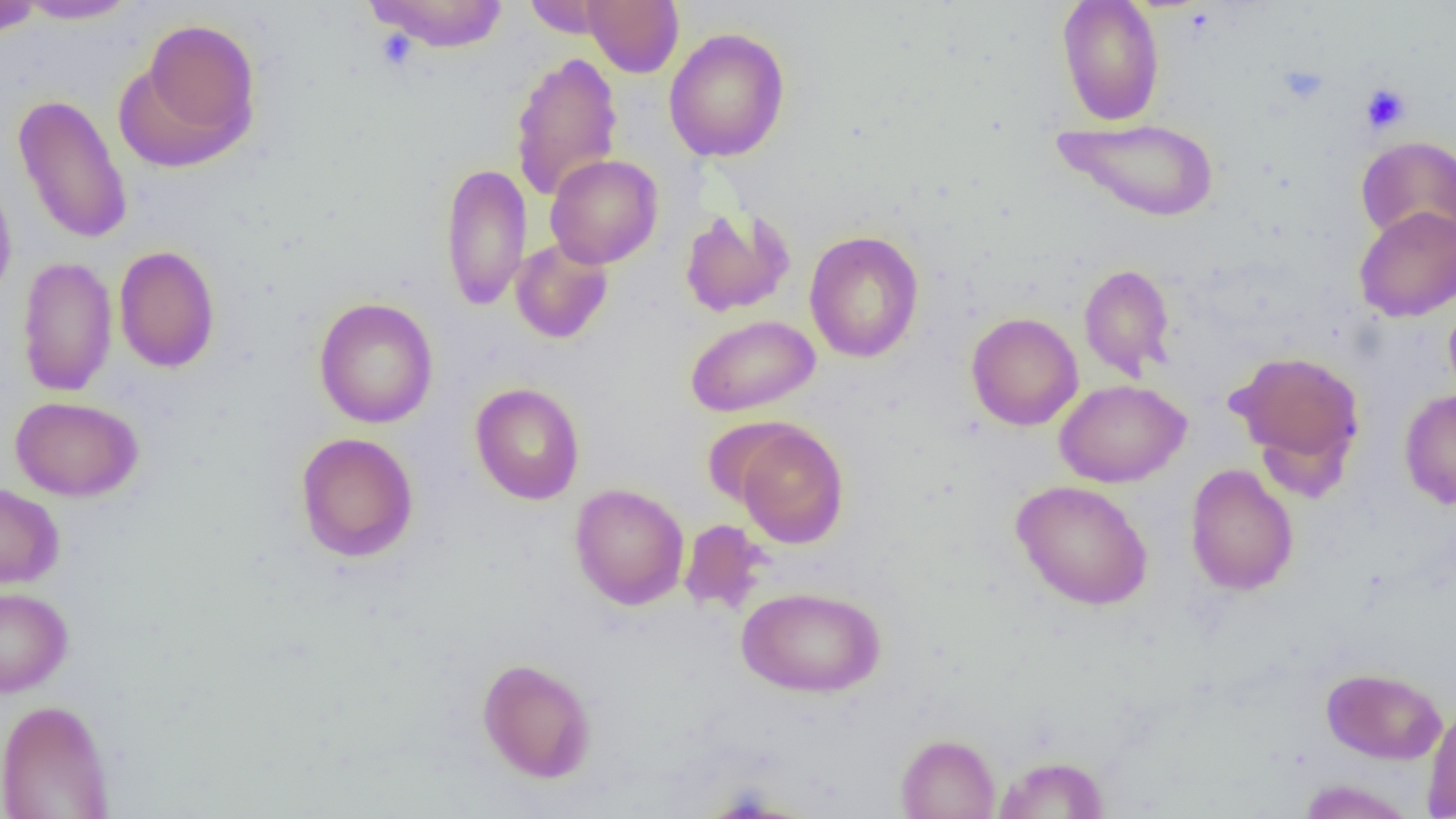

Summary:
  - Coordinate format: approximate bounding boxes as (x1, y1, x2, y2) in pixels
  - Platelet locations: (1277, 65, 1329, 105), (1360, 83, 1411, 134)
  - Uninfected red blood cell locations: (364, 0, 510, 52), (522, 0, 615, 38), (582, 0, 683, 77), (1057, 0, 1165, 126), (0, 1, 43, 38), (15, 1, 141, 24), (135, 17, 261, 162), (663, 28, 791, 162), (509, 51, 623, 202), (12, 92, 133, 246), (1053, 117, 1220, 223), (1356, 136, 1456, 244), (545, 154, 663, 269), (440, 162, 532, 311), (0, 172, 17, 303), (1354, 206, 1456, 322), (679, 207, 796, 317), (804, 230, 924, 363), (510, 238, 613, 344), (114, 245, 220, 373), (17, 255, 117, 396), (1079, 263, 1176, 380), (1444, 294, 1456, 406), (313, 297, 439, 428), (966, 312, 1083, 431), (685, 314, 820, 417), (1227, 349, 1365, 478), (1055, 379, 1191, 488), (470, 383, 585, 505), (1399, 389, 1456, 509), (10, 396, 144, 501), (701, 417, 803, 508), (733, 420, 849, 548), (295, 432, 419, 562), (1185, 464, 1299, 595), (1011, 479, 1153, 611), (0, 482, 64, 590), (570, 483, 689, 610), (679, 518, 770, 615), (736, 585, 886, 697), (0, 587, 73, 698), (476, 657, 597, 783), (1321, 667, 1447, 764), (0, 698, 115, 819), (1422, 703, 1456, 818), (895, 733, 1000, 818), (994, 755, 1110, 818), (1297, 779, 1417, 819)
  - Slide-level diagnosis: no evidence of blood parasites
  - Modality: light microscopy
  - Preparation: thin blood film
  - Field of view: one of a larger specimen
  - Magnification: 1000x
  - Image size: 1456×819 pixels